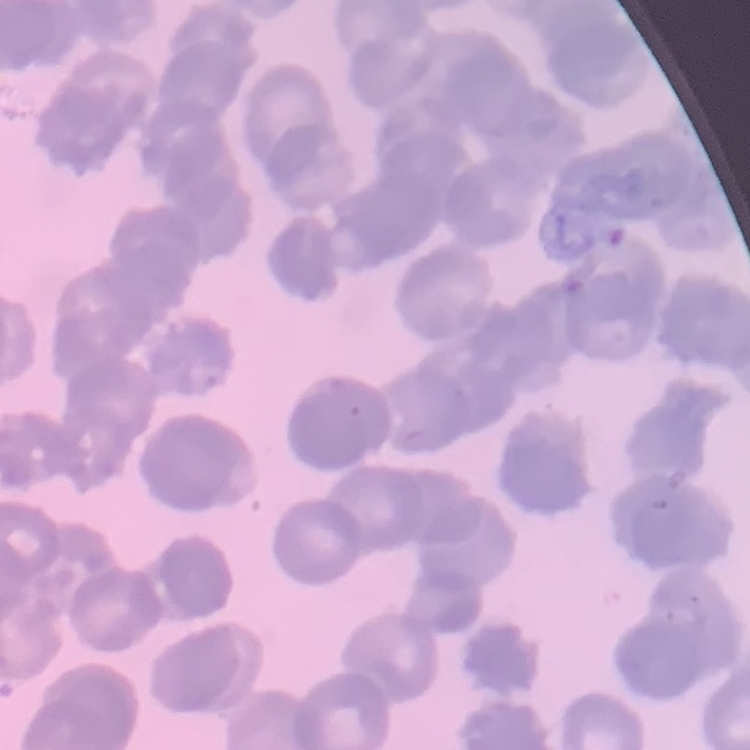

Summary:
  - Erythrocyte morphology: rouleaux formation
  - Stain: Field's or Giemsa
  - Preparation: thin blood film
  - Image type: square crop of a larger photomicrograph